Point out each Plasmodium parasite.
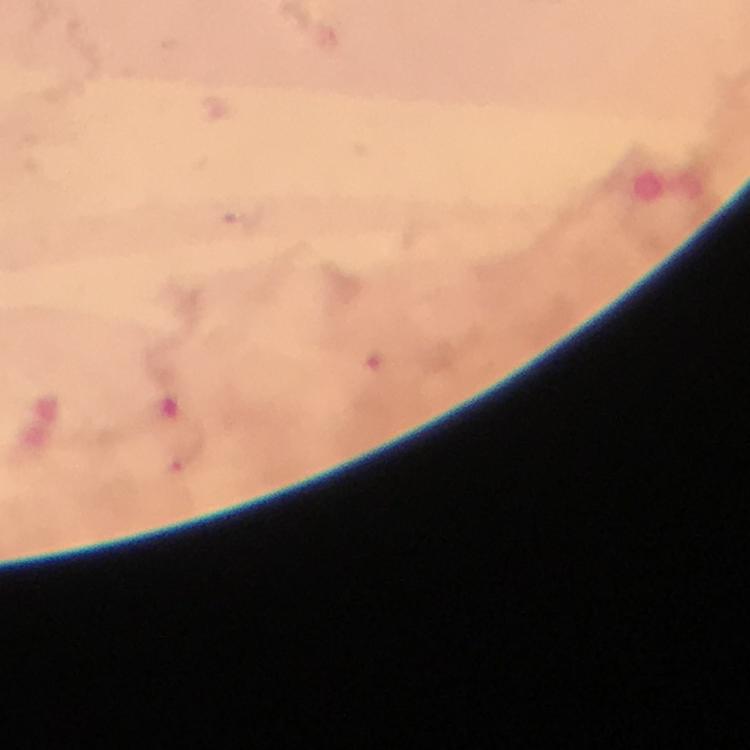

Approximate centers as [x, y] in pixels.
Plasmodium parasites: [184, 456].

stain = Giemsa
magnification = 100x
image size = 750×750 pixels
context = from a malaria diagnostic workup
cropped from = a single field of view
capture = smartphone photograph through a microscope
immersion oil = used
preparation = thick blood smear